Point out each malaria parasite.
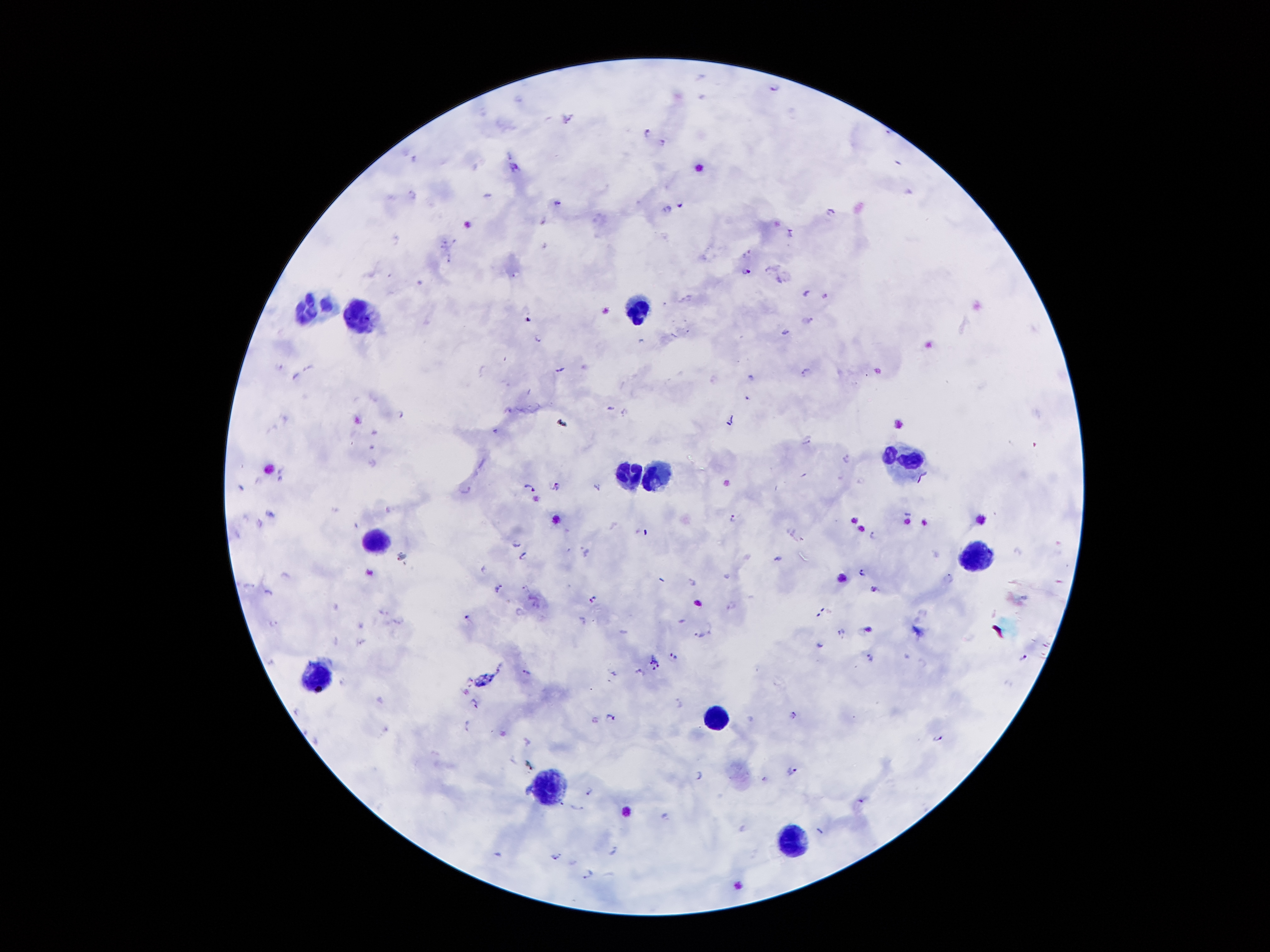

Approximate object centers, in pixels from the top-left corner.
Malaria parasites: (x=776, y=86), (x=566, y=117), (x=647, y=132), (x=662, y=141), (x=413, y=157), (x=514, y=165), (x=410, y=192), (x=558, y=204), (x=680, y=205), (x=669, y=208), (x=832, y=211), (x=541, y=222), (x=791, y=232), (x=749, y=254), (x=745, y=269), (x=779, y=278), (x=806, y=292), (x=825, y=294), (x=809, y=319), (x=785, y=330), (x=539, y=336), (x=280, y=363), (x=559, y=366), (x=308, y=367), (x=805, y=370), (x=292, y=376), (x=750, y=376), (x=747, y=397), (x=610, y=407), (x=403, y=413), (x=624, y=413), (x=806, y=439), (x=847, y=457), (x=530, y=486), (x=554, y=486), (x=598, y=486), (x=467, y=489), (x=733, y=517), (x=258, y=522), (x=873, y=536), (x=516, y=541), (x=584, y=550), (x=522, y=555), (x=402, y=556), (x=778, y=558), (x=863, y=573), (x=948, y=577), (x=693, y=583), (x=246, y=584), (x=525, y=586), (x=498, y=587), (x=873, y=588), (x=268, y=592), (x=593, y=598), (x=732, y=604), (x=384, y=611), (x=519, y=612), (x=467, y=615), (x=399, y=619), (x=582, y=620), (x=273, y=622), (x=709, y=627), (x=842, y=632), (x=696, y=635), (x=336, y=640), (x=672, y=656), (x=870, y=657), (x=1024, y=658), (x=655, y=664), (x=639, y=672), (x=526, y=673), (x=613, y=673), (x=469, y=678), (x=341, y=681), (x=476, y=702), (x=679, y=702), (x=297, y=709), (x=792, y=714), (x=612, y=718), (x=594, y=719), (x=468, y=723), (x=937, y=738), (x=790, y=770), (x=699, y=775), (x=765, y=779), (x=588, y=792), (x=576, y=806), (x=664, y=815), (x=818, y=829), (x=614, y=850), (x=555, y=856), (x=589, y=873).

Leukocyte locations: (x=317, y=305), (x=638, y=308), (x=370, y=317), (x=907, y=461), (x=657, y=475), (x=631, y=476), (x=373, y=539), (x=975, y=556), (x=320, y=671), (x=715, y=717), (x=547, y=786), (x=791, y=841). Smartphone photograph taken through the microscope eyepiece. Patient malaria status: infected with Plasmodium falciparum. 100x magnification. Thick blood film. Giemsa stain. Single field of view. Image is 1270×952 pixels.